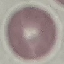
Summary:
  - Result: negative for malaria parasites
  - Stain: Giemsa
  - Image type: automatically extracted cell patch, resized to 64 × 64 pixels
  - Preparation: thin blood film
  - Capture: smartphone camera at the microscope eyepiece